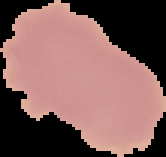
Image is 166×157 pixels. Result: no Plasmodium parasites detected. The area outside the segmented cell region is set to black. From a thin blood film.